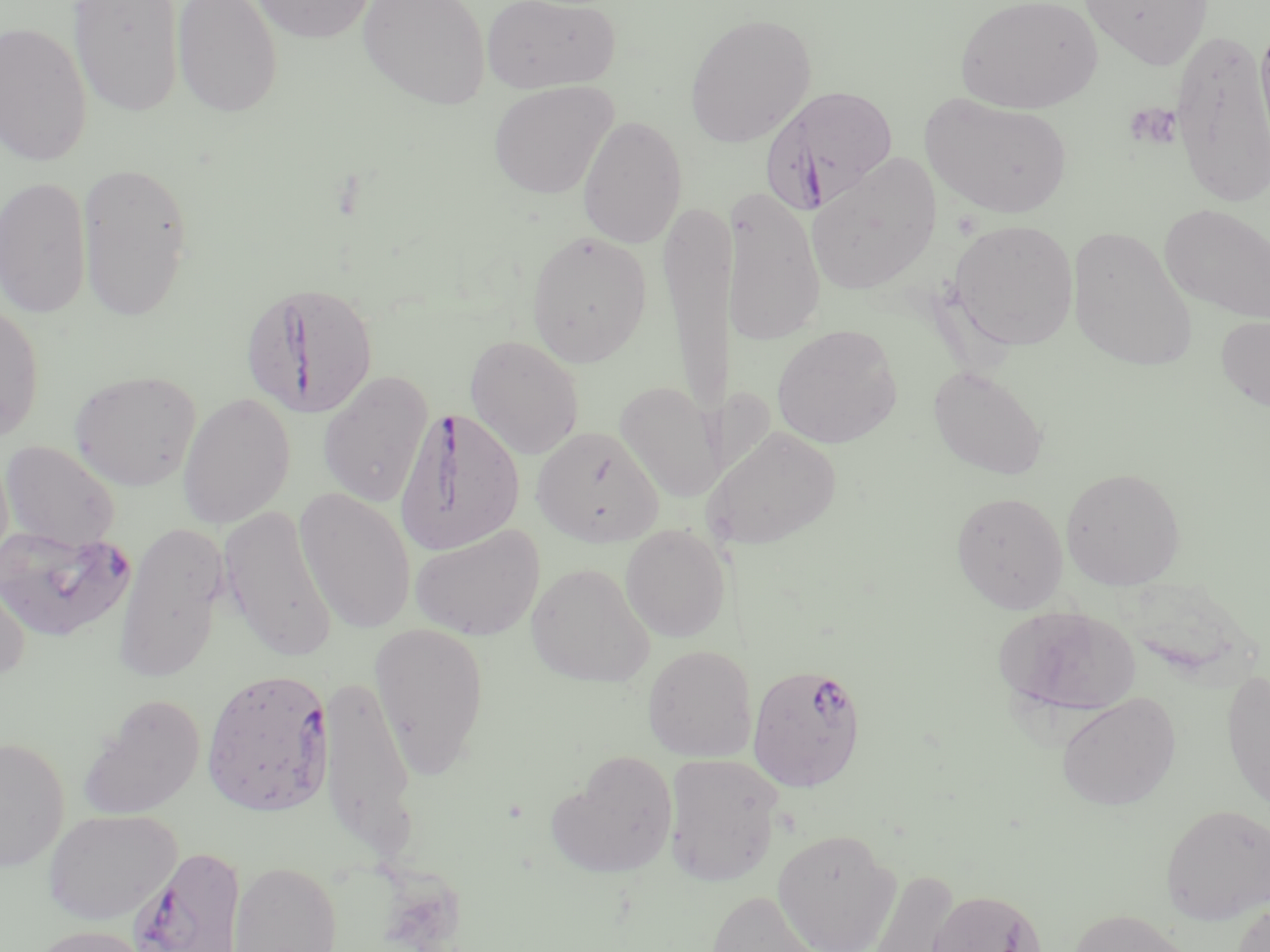

Approximate bounding boxes as named x1/y1/x2/y2 corners in pixels. Platelet locations: (x1=1123, y1=101, x2=1182, y2=151). Uninfected red blood cell locations: (x1=68, y1=0, x2=184, y2=117), (x1=171, y1=0, x2=283, y2=118), (x1=251, y1=0, x2=376, y2=43), (x1=358, y1=0, x2=491, y2=109), (x1=481, y1=0, x2=621, y2=94), (x1=955, y1=0, x2=1103, y2=114), (x1=1080, y1=1, x2=1213, y2=71), (x1=684, y1=12, x2=816, y2=148), (x1=1254, y1=17, x2=1270, y2=166), (x1=0, y1=20, x2=93, y2=167), (x1=1170, y1=28, x2=1270, y2=211), (x1=489, y1=81, x2=618, y2=199), (x1=920, y1=92, x2=1072, y2=218), (x1=577, y1=115, x2=687, y2=249), (x1=806, y1=153, x2=942, y2=295), (x1=77, y1=162, x2=193, y2=322), (x1=0, y1=174, x2=92, y2=320), (x1=721, y1=186, x2=826, y2=346), (x1=658, y1=201, x2=735, y2=420), (x1=1159, y1=203, x2=1270, y2=324), (x1=948, y1=219, x2=1079, y2=350), (x1=1066, y1=225, x2=1197, y2=371), (x1=525, y1=229, x2=652, y2=367), (x1=0, y1=301, x2=44, y2=442), (x1=1215, y1=313, x2=1270, y2=413), (x1=771, y1=323, x2=903, y2=449), (x1=465, y1=334, x2=584, y2=459), (x1=928, y1=365, x2=1049, y2=480), (x1=69, y1=369, x2=201, y2=491), (x1=317, y1=370, x2=434, y2=508), (x1=614, y1=380, x2=723, y2=502), (x1=716, y1=385, x2=778, y2=485), (x1=177, y1=391, x2=296, y2=529), (x1=532, y1=426, x2=664, y2=548), (x1=704, y1=426, x2=842, y2=550), (x1=0, y1=440, x2=121, y2=551), (x1=1062, y1=467, x2=1186, y2=590), (x1=295, y1=486, x2=417, y2=633), (x1=950, y1=490, x2=1068, y2=613), (x1=220, y1=504, x2=337, y2=661), (x1=112, y1=521, x2=229, y2=681), (x1=409, y1=523, x2=544, y2=640), (x1=620, y1=524, x2=731, y2=642), (x1=526, y1=561, x2=655, y2=688), (x1=0, y1=569, x2=32, y2=684), (x1=995, y1=605, x2=1141, y2=719), (x1=369, y1=622, x2=490, y2=777), (x1=642, y1=644, x2=757, y2=762), (x1=1221, y1=668, x2=1269, y2=813), (x1=317, y1=673, x2=418, y2=862), (x1=1056, y1=692, x2=1181, y2=810), (x1=78, y1=694, x2=205, y2=820), (x1=0, y1=736, x2=69, y2=870), (x1=547, y1=750, x2=678, y2=878), (x1=663, y1=752, x2=785, y2=887), (x1=1160, y1=803, x2=1270, y2=924), (x1=43, y1=808, x2=182, y2=925), (x1=773, y1=828, x2=900, y2=952), (x1=229, y1=860, x2=342, y2=952), (x1=866, y1=868, x2=959, y2=952), (x1=701, y1=888, x2=827, y2=952), (x1=926, y1=888, x2=1047, y2=952), (x1=1231, y1=900, x2=1270, y2=952), (x1=1067, y1=908, x2=1197, y2=952), (x1=24, y1=923, x2=156, y2=952). Plasmodium falciparum-infected red blood cell locations: (x1=762, y1=84, x2=899, y2=214), (x1=241, y1=280, x2=379, y2=420), (x1=395, y1=405, x2=525, y2=556), (x1=1, y1=524, x2=137, y2=642), (x1=746, y1=661, x2=867, y2=791), (x1=201, y1=667, x2=335, y2=818), (x1=128, y1=846, x2=247, y2=952). Slide-level diagnosis: Plasmodium falciparum. Thin blood film. May-Grünwald-Giemsa-stained preparation. Single field of view. 1000x magnification. Image is 1270×952 pixels. Light microscopy.